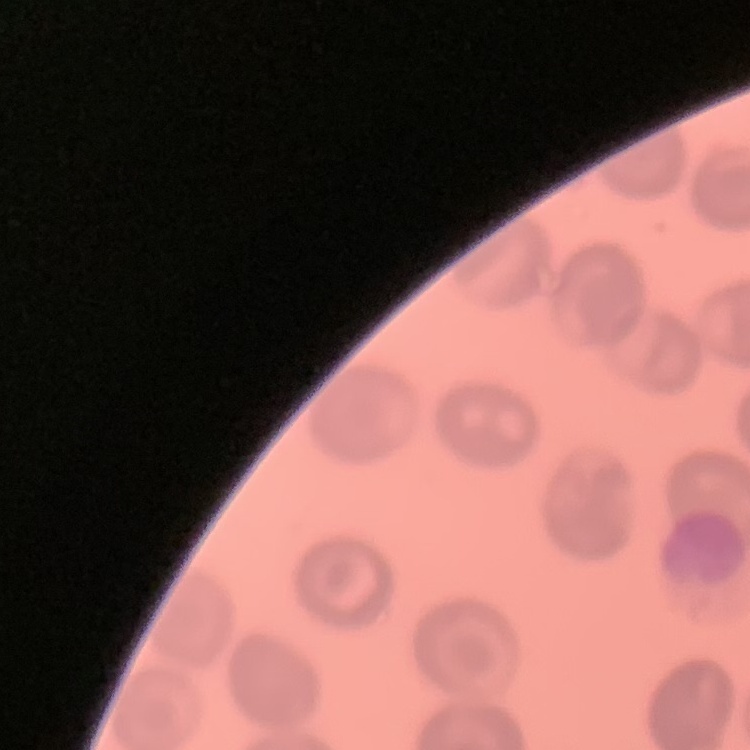

The red blood cells show no rouleaux formation. Field's or Giemsa stain. One tile cut from a larger photomicrograph. Thin blood smear.